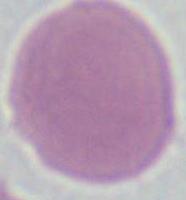

Summary:
  - Identification: erythrocyte
  - Magnification: 1000x
  - Modality: micrograph